Assess this cell for malaria.
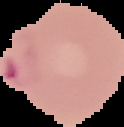
It is parasitized.

Segmented cell region on a black background. From a thin blood film. Image is 124×127 pixels.